Locate and identify every blood parasite.
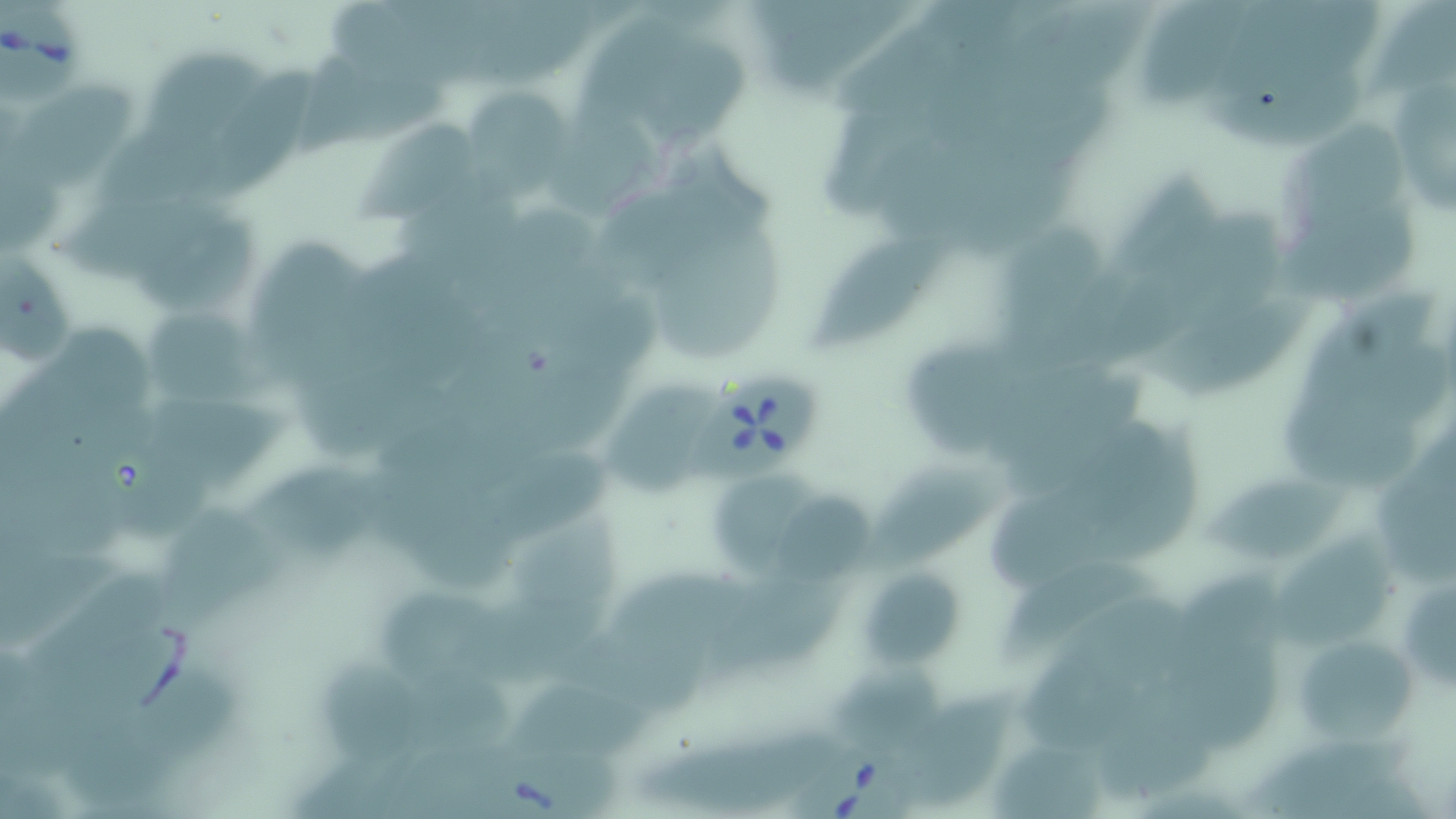

Approximate bounding boxes as (x1, y1, x2, y2) in pixels.
Babesia divergens-infected red blood cells: (2, 4, 81, 110), (684, 376, 826, 481), (469, 735, 616, 819), (797, 736, 915, 819).
No Plasmodium falciparum, Plasmodium ovale, Plasmodium malariae, Plasmodium vivax, or Trypanosoma brucei observed.

slide_level_diagnosis: Babesia divergens
stain: May-Grünwald-Giemsa
image_size: 1456×819 pixels
field_of_view: single
uninfected_red_blood_cell_locations: 'approximate bounding boxes as (x1, y1, x2, y2) in pixels: (1146, 2, 1256, 106), (632, 25, 753, 145), (140, 42, 259, 148), (1381, 50, 1456, 223), (295, 51, 448, 162), (206, 62, 315, 200), (15, 82, 139, 196), (468, 90, 581, 204), (1284, 119, 1410, 245), (351, 120, 481, 226), (128, 205, 268, 319), (651, 206, 788, 365), (992, 217, 1126, 367), (807, 231, 948, 351), (257, 240, 377, 394), (1141, 288, 1312, 403), (150, 308, 259, 408), (909, 339, 1038, 462), (1282, 379, 1429, 492), (609, 382, 723, 497), (1079, 433, 1204, 579), (475, 448, 614, 556), (866, 458, 1033, 578), (257, 461, 405, 567), (1200, 464, 1357, 568), (715, 480, 823, 579), (775, 491, 877, 584), (159, 499, 288, 635), (515, 511, 623, 677), (1262, 527, 1399, 656), (994, 555, 1167, 657), (1157, 562, 1282, 690), (711, 567, 853, 682), (857, 567, 969, 669), (380, 584, 512, 683), (1298, 627, 1413, 753), (837, 664, 944, 752), (901, 697, 1032, 812), (630, 716, 843, 812), (990, 741, 1103, 819), (1264, 741, 1436, 818)'
modality: optical microscopy
magnification: 1000x
preparation: thin blood smear